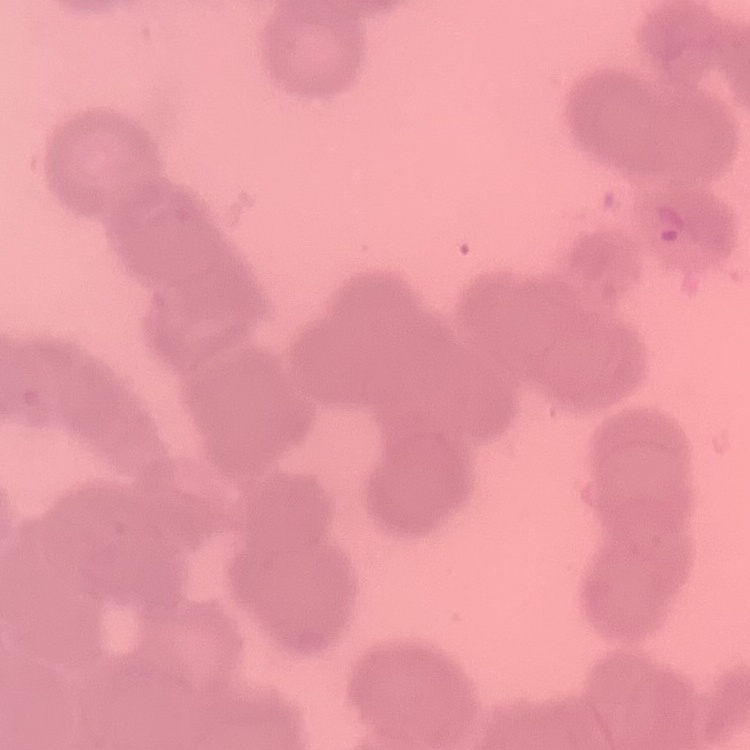
red_blood_cell_morphology: rouleaux formation
image_type: one tile cut from a larger photomicrograph
stain: Field's or Giemsa
preparation: thin peripheral smear